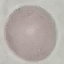
result = negative for malaria parasites
capture = smartphone camera at the microscope eyepiece
preparation = thin blood film
image type = automatically extracted cell patch, resized to 64 × 64 pixels
stain = Giemsa